Give the extent of all Plasmodium vivax-infected red blood cells.
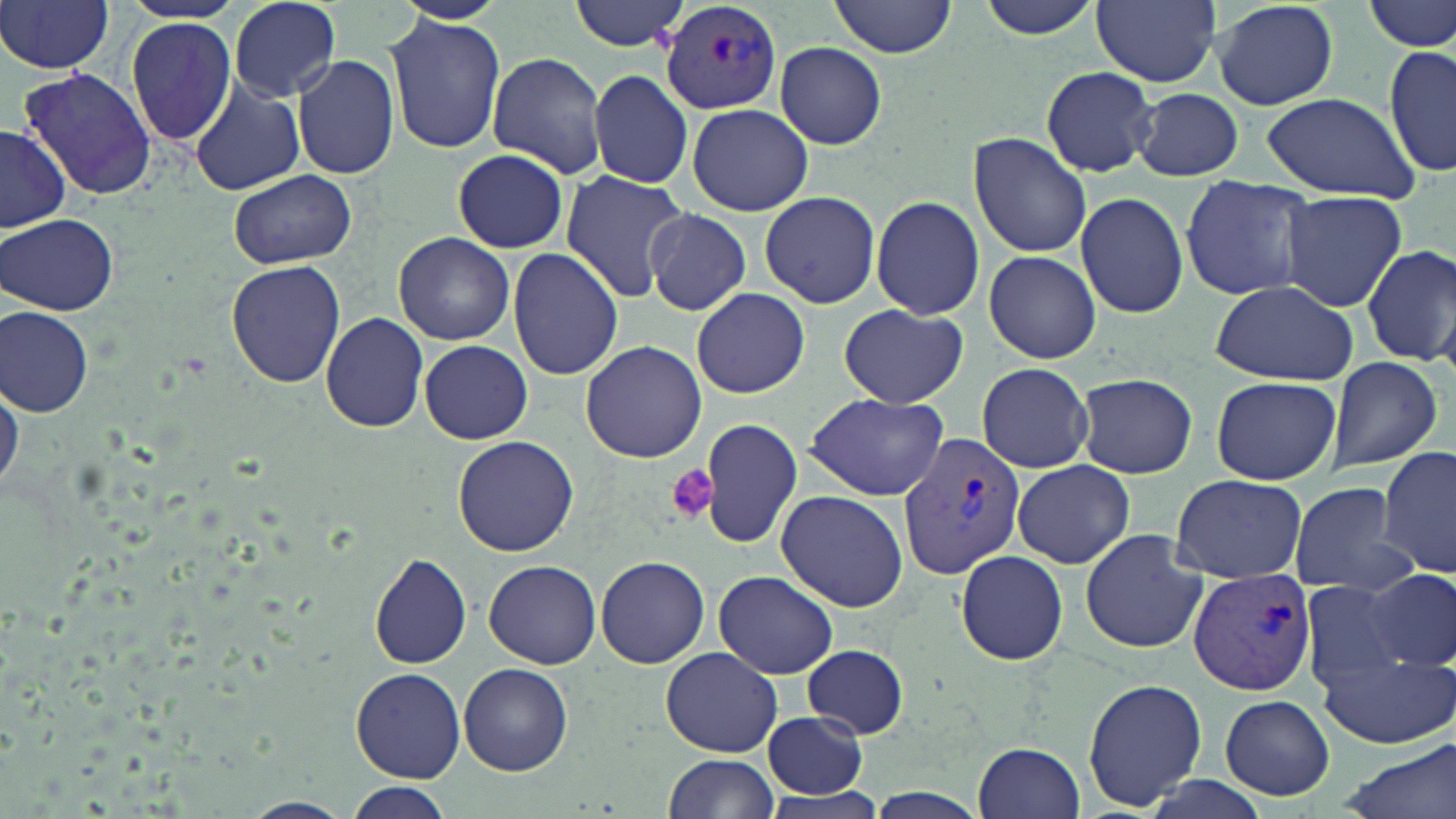

Approximate bounding boxes as named x1/y1/x2/y2 corners in pixels.
Plasmodium vivax-infected red blood cells: (x1=661, y1=2, x2=782, y2=114), (x1=895, y1=430, x2=1027, y2=581), (x1=1188, y1=568, x2=1317, y2=696).

Uninfected red blood cell locations: (x1=390, y1=0, x2=509, y2=26), (x1=570, y1=0, x2=694, y2=52), (x1=831, y1=0, x2=956, y2=58), (x1=975, y1=0, x2=1104, y2=40), (x1=1092, y1=0, x2=1220, y2=87), (x1=1211, y1=0, x2=1340, y2=111), (x1=1367, y1=0, x2=1456, y2=54), (x1=1, y1=1, x2=115, y2=75), (x1=228, y1=1, x2=343, y2=102), (x1=384, y1=13, x2=506, y2=155), (x1=125, y1=20, x2=238, y2=145), (x1=775, y1=41, x2=887, y2=149), (x1=1383, y1=44, x2=1455, y2=179), (x1=486, y1=52, x2=609, y2=179), (x1=292, y1=55, x2=399, y2=179), (x1=18, y1=66, x2=156, y2=200), (x1=1040, y1=66, x2=1159, y2=176), (x1=588, y1=69, x2=694, y2=188), (x1=521, y1=74, x2=664, y2=190), (x1=190, y1=81, x2=306, y2=197), (x1=1134, y1=88, x2=1242, y2=181), (x1=1259, y1=91, x2=1425, y2=204), (x1=687, y1=103, x2=812, y2=216), (x1=0, y1=123, x2=72, y2=232), (x1=969, y1=133, x2=1091, y2=257), (x1=451, y1=148, x2=569, y2=255), (x1=228, y1=169, x2=356, y2=268), (x1=560, y1=172, x2=692, y2=303), (x1=1179, y1=176, x2=1320, y2=301), (x1=759, y1=190, x2=881, y2=309), (x1=1279, y1=190, x2=1409, y2=313), (x1=1075, y1=191, x2=1189, y2=319), (x1=870, y1=195, x2=985, y2=320), (x1=643, y1=208, x2=752, y2=315), (x1=2, y1=213, x2=121, y2=316), (x1=392, y1=232, x2=514, y2=346), (x1=1361, y1=244, x2=1456, y2=369), (x1=508, y1=247, x2=624, y2=381), (x1=984, y1=250, x2=1100, y2=364), (x1=226, y1=259, x2=346, y2=389), (x1=1208, y1=281, x2=1357, y2=387), (x1=691, y1=288, x2=811, y2=399), (x1=838, y1=303, x2=970, y2=407), (x1=1, y1=305, x2=94, y2=416), (x1=320, y1=312, x2=428, y2=432), (x1=579, y1=338, x2=707, y2=463), (x1=420, y1=340, x2=532, y2=444), (x1=1327, y1=358, x2=1441, y2=470), (x1=976, y1=362, x2=1095, y2=472), (x1=1, y1=372, x2=22, y2=499), (x1=1072, y1=372, x2=1197, y2=479), (x1=1211, y1=376, x2=1340, y2=486), (x1=805, y1=394, x2=952, y2=500), (x1=699, y1=418, x2=803, y2=550), (x1=453, y1=434, x2=580, y2=557), (x1=1379, y1=446, x2=1456, y2=579), (x1=1011, y1=460, x2=1134, y2=568), (x1=1171, y1=475, x2=1310, y2=584), (x1=1288, y1=481, x2=1418, y2=598), (x1=775, y1=490, x2=910, y2=612), (x1=1078, y1=529, x2=1208, y2=652), (x1=954, y1=548, x2=1069, y2=664), (x1=370, y1=554, x2=471, y2=669), (x1=596, y1=556, x2=710, y2=668), (x1=485, y1=561, x2=600, y2=670), (x1=1361, y1=568, x2=1456, y2=671), (x1=713, y1=571, x2=839, y2=680), (x1=1299, y1=579, x2=1414, y2=690), (x1=802, y1=644, x2=908, y2=738), (x1=660, y1=647, x2=782, y2=757), (x1=1319, y1=649, x2=1456, y2=749), (x1=459, y1=663, x2=572, y2=776), (x1=350, y1=667, x2=465, y2=783), (x1=1082, y1=678, x2=1209, y2=813), (x1=1219, y1=695, x2=1335, y2=802), (x1=761, y1=711, x2=868, y2=799), (x1=1341, y1=739, x2=1456, y2=819), (x1=972, y1=740, x2=1085, y2=819), (x1=661, y1=754, x2=781, y2=818), (x1=341, y1=782, x2=455, y2=818), (x1=239, y1=798, x2=353, y2=819). Platelet locations: (x1=667, y1=465, x2=722, y2=524). Slide-level diagnosis: Plasmodium vivax. Thin blood smear. May-Grünwald-Giemsa stain. One field of a larger specimen. Optical microscopy. Image is 1456×819 pixels. 1000x magnification.